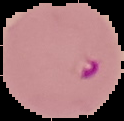
Summary:
  - Image size: 124×121 pixels
  - Image type: cell region segmented out of the field of view; surrounding area masked to black
  - Preparation: thin blood film
  - Malaria status: parasitized